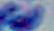
magnification = 1000x
identification = Toxoplasma gondii
modality = micrograph